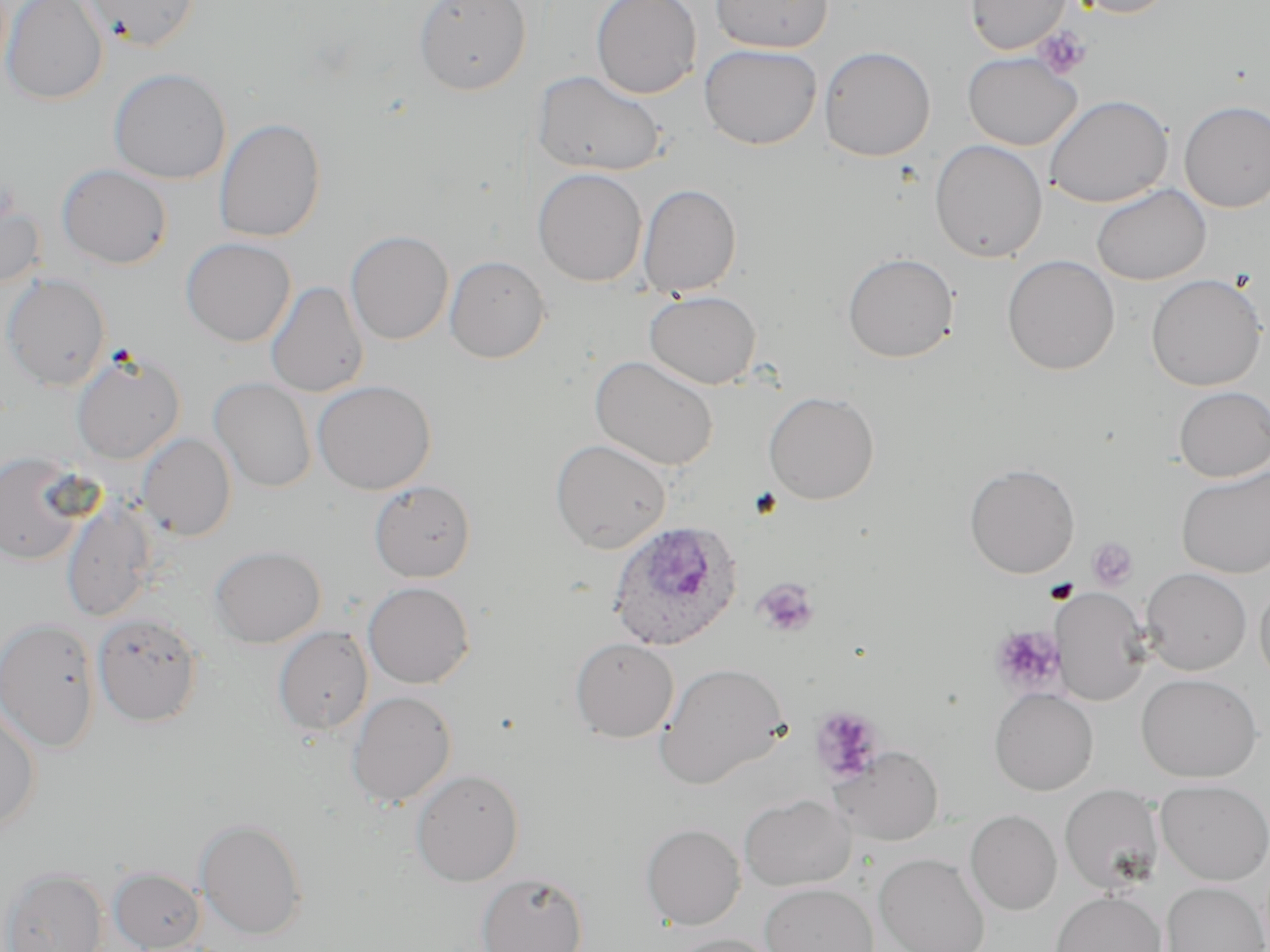

Summary:
  - Coordinate format: approximate bounding boxes as (x1, y1, x2, y2) in pixels
  - Platelet locations: (1034, 26, 1092, 80), (1087, 537, 1138, 591), (753, 579, 819, 638), (990, 625, 1064, 695), (810, 706, 884, 784)
  - Plasmodium ovale-infected red blood cell locations: (607, 520, 742, 652)
  - Uninfected red blood cell locations: (1, 0, 108, 105), (82, 0, 201, 51), (413, 0, 531, 95), (590, 0, 702, 99), (710, 0, 833, 53), (965, 0, 1071, 54), (1061, 0, 1178, 18), (699, 43, 823, 150), (818, 46, 936, 162), (961, 52, 1082, 150), (108, 67, 231, 184), (533, 70, 666, 177), (1044, 94, 1173, 208), (1179, 100, 1270, 213), (214, 117, 326, 243), (929, 139, 1048, 263), (56, 164, 172, 269), (533, 168, 647, 286), (638, 183, 742, 297), (1091, 183, 1211, 285), (0, 187, 45, 290), (345, 230, 453, 345), (180, 237, 296, 347), (842, 252, 959, 363), (444, 254, 551, 363), (1002, 255, 1119, 375), (2, 273, 111, 391), (1146, 274, 1267, 391), (265, 281, 369, 398), (644, 290, 761, 389), (71, 352, 186, 464), (590, 355, 719, 471), (209, 378, 317, 493), (312, 379, 436, 495), (1173, 386, 1270, 481), (763, 390, 880, 504), (137, 433, 236, 541), (550, 438, 672, 553), (0, 451, 94, 566), (964, 463, 1080, 578), (1176, 466, 1270, 579), (369, 480, 476, 582), (61, 501, 158, 623), (209, 545, 326, 648), (1140, 567, 1252, 675), (1255, 580, 1270, 689), (363, 581, 474, 688), (1051, 586, 1152, 706), (92, 613, 203, 726), (0, 617, 101, 753), (273, 626, 373, 735), (570, 637, 679, 742), (656, 662, 790, 789), (1136, 672, 1264, 783), (989, 688, 1098, 795), (346, 691, 457, 808), (0, 704, 41, 832), (831, 746, 944, 845), (410, 768, 524, 886), (1156, 780, 1270, 885), (1059, 784, 1164, 894), (739, 793, 855, 891), (965, 809, 1062, 915), (196, 818, 308, 940), (641, 823, 745, 930), (874, 853, 991, 952), (1, 867, 108, 952), (109, 867, 206, 951), (476, 872, 588, 952), (1161, 881, 1269, 952), (760, 882, 878, 952), (1050, 891, 1167, 952), (665, 934, 782, 952)
  - Slide-level diagnosis: Plasmodium ovale
  - Preparation: thin blood smear
  - Stain: May-Grünwald-Giemsa
  - Image size: 1270×952 pixels
  - Modality: light microscopy
  - Magnification: 1000x
  - Field of view: one of a larger specimen